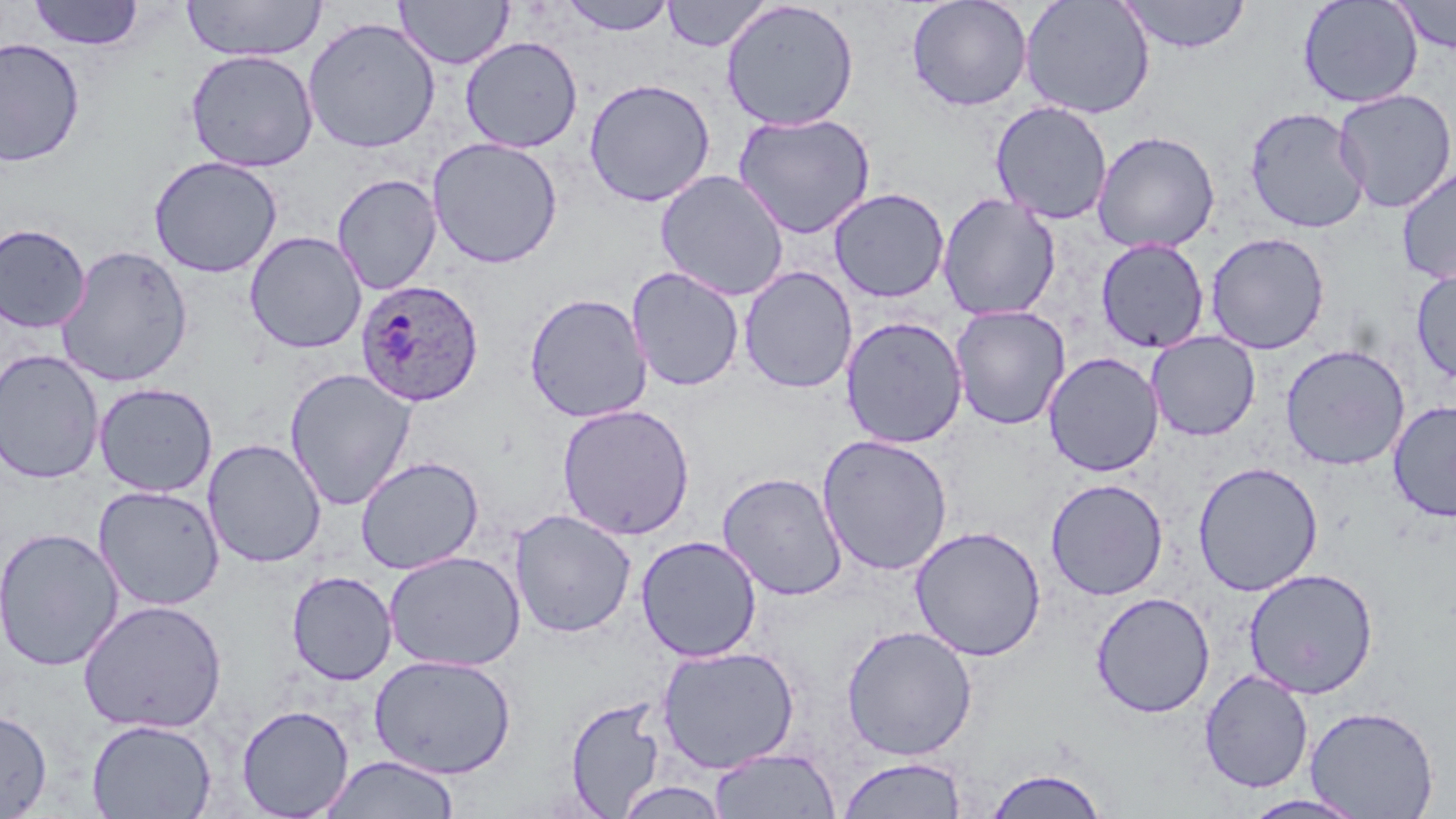
slide_level_diagnosis: Plasmodium ovale
modality: light microscopy
plasmodium_ovale_infected_red_blood_cell_locations: 'approximate bounding boxes as (x1,y1)-(x2,y2) corner pairs in pixels: (355,279)-(484,407)'
stain: May-Grünwald-Giemsa
uninfected_red_blood_cell_locations: 'approximate bounding boxes as (x1,y1)-(x2,y2) corner pairs in pixels: (29,0)-(144,50), (181,0)-(325,62), (394,0)-(514,69), (557,0)-(677,36), (906,0)-(1033,112), (1020,0)-(1155,119), (1118,0)-(1251,54), (1297,0)-(1423,108), (1390,0)-(1455,55), (663,1)-(771,52), (720,1)-(860,131), (303,16)-(441,154), (460,36)-(583,153), (0,38)-(86,168), (184,49)-(319,172), (583,78)-(716,207), (1332,89)-(1456,213), (990,100)-(1112,224), (1243,107)-(1370,233), (732,112)-(876,239), (1092,130)-(1220,253), (427,137)-(563,269), (148,155)-(283,278), (1396,165)-(1456,285), (655,169)-(790,301), (332,173)-(442,294), (828,187)-(950,303), (937,192)-(1061,321), (0,224)-(91,333), (244,231)-(367,354), (1205,232)-(1329,354), (1095,238)-(1209,353), (55,245)-(193,387), (738,266)-(858,394), (1411,266)-(1456,385), (626,267)-(745,392), (524,292)-(653,423), (949,305)-(1070,430), (840,316)-(968,449), (1146,331)-(1261,441), (1280,344)-(1410,470), (0,349)-(104,485), (1043,351)-(1164,477), (284,368)-(417,510), (94,382)-(218,497), (1387,399)-(1456,521), (556,403)-(695,540), (817,433)-(954,576), (203,438)-(327,568), (355,455)-(484,575), (1192,461)-(1324,596), (717,471)-(848,601), (1045,478)-(1169,601), (93,485)-(226,611), (509,509)-(637,638), (909,525)-(1047,661), (0,526)-(124,672), (636,535)-(762,663), (384,550)-(526,672), (1242,567)-(1379,699), (286,570)-(398,686), (1090,591)-(1215,719), (77,599)-(228,735), (840,624)-(978,760), (655,644)-(801,774), (368,654)-(517,779), (1199,669)-(1313,793), (564,696)-(667,816), (236,704)-(355,818), (1305,705)-(1440,818), (0,709)-(52,817), (86,718)-(216,818), (708,747)-(841,818), (318,754)-(461,818), (837,756)-(968,818), (982,765)-(1110,818), (614,780)-(730,819), (1239,793)-(1370,818)'
magnification: 1000x
image_size: 1456×819 pixels
preparation: thin blood smear
field_of_view: one of a larger specimen